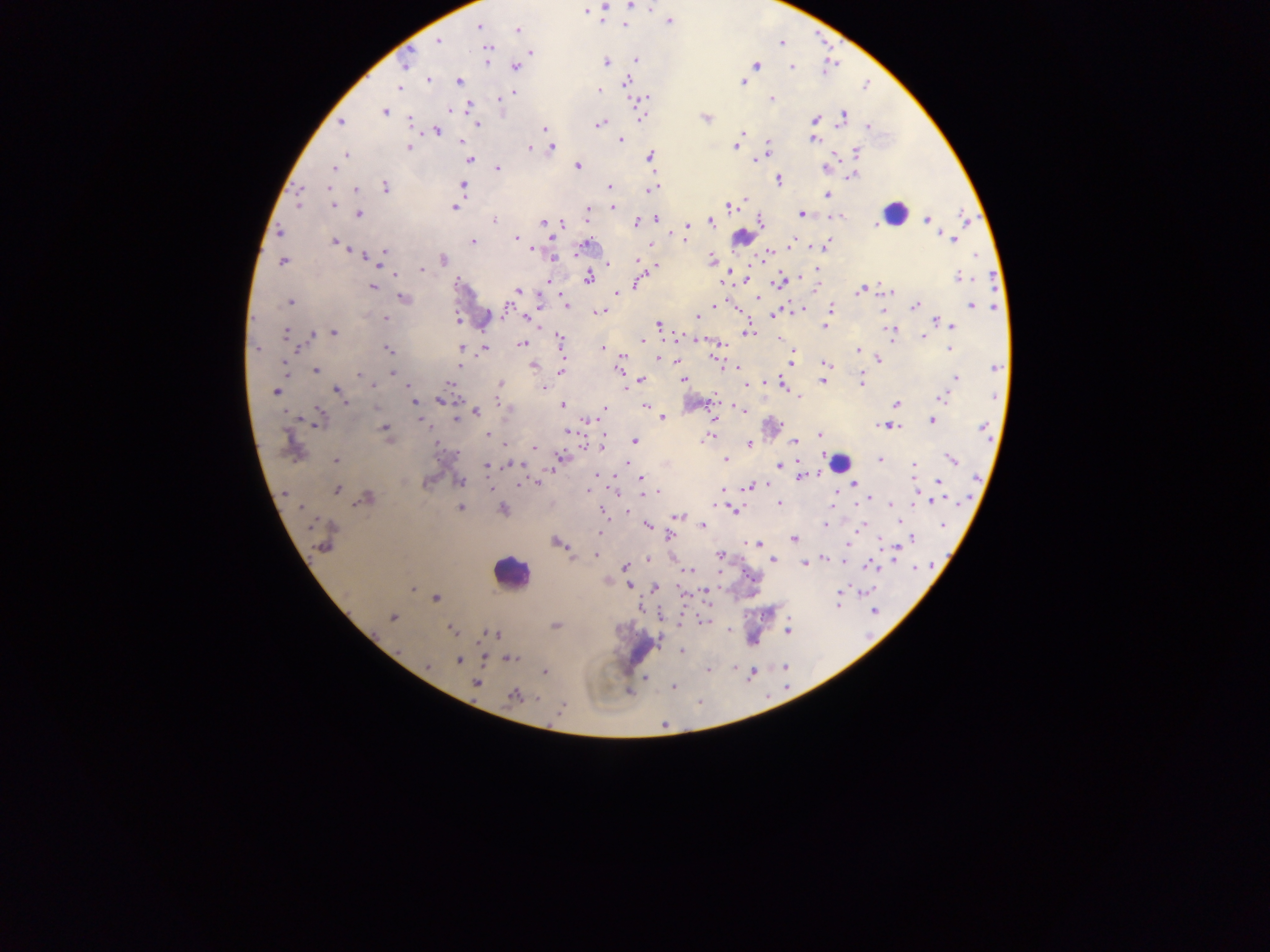

capture = mobile-phone photograph through a microscope
preparation = thick blood smear
field of view = single
image size = 1270×952 pixels
country = Ghana
leukocyte locations = approximate centers as x y in pixels (subset; some below the resolvable size): 896 214; 742 238; 478 310; 841 462; 511 572; 642 650
malaria parasite locations = approximate centers as x y in pixels: 634 5; 604 7; 585 11; 670 21; 625 24; 478 27; 518 29; 438 40; 485 44; 487 52; 531 52; 635 59; 487 60; 405 62; 605 62; 757 65; 516 67; 792 67; 428 80; 459 81; 626 82; 743 82; 399 88; 598 91; 513 93; 503 97; 772 98; 645 99; 468 107; 384 111; 450 111; 640 114; 843 115; 705 118; 814 119; 341 122; 409 122; 477 124; 600 124; 869 126; 544 128; 437 130; 741 132; 622 140; 813 140; 461 142; 767 144; 735 146; 408 147; 529 148; 552 148; 856 152; 346 154; 649 157; 760 157; 470 159; 756 159; 578 166; 334 168; 497 168; 826 168; 854 175; 779 180; 463 185; 329 186; 386 187; 609 188; 356 189; 651 190; 827 195; 297 203; 333 206; 730 206; 455 207; 612 207; 588 212; 359 214; 801 214; 840 216; 655 219; 964 219; 927 220; 494 221; 544 222; 637 222; 711 222; 760 222; 562 223; 877 224; 687 225; 280 232; 685 238; 516 239; 953 239; 475 241; 336 242; 792 243; 586 245; 650 245; 826 245; 532 250; 385 252; 766 254; 364 255; 553 258; 711 259; 443 260; 638 260; 282 261; 608 264; 654 266; 421 270; 395 274; 960 277; 588 278; 548 280; 746 280; 457 281; 778 282; 637 283; 372 287; 814 288; 885 289; 859 290; 518 291; 889 292; 616 293; 403 298; 757 298; 290 302; 566 305; 915 305; 973 305; 714 306; 738 309; 830 309; 505 311; 602 311; 883 311; 773 315; 529 317; 696 317; 386 318; 456 321; 658 325; 949 325; 824 326; 890 331; 334 333; 748 333; 285 334; 312 335; 923 336; 680 338; 780 338; 561 339; 642 340; 522 343; 258 348; 462 348; 484 348; 602 348; 950 349; 388 350; 857 350; 621 357; 658 358; 715 358; 878 360; 677 362; 792 362; 285 364; 825 364; 459 367; 534 367; 996 367; 736 368; 619 370; 315 371; 562 371; 392 372; 358 375; 362 375; 956 378; 684 379; 641 380; 823 381; 862 382; 449 383; 501 383; 782 384; 373 385; 746 385; 409 387; 544 387; 337 390; 275 391; 799 396; 942 398; 439 400; 414 402; 498 402; 346 403; 896 403; 563 405; 646 407; 605 408; 741 410; 475 411; 663 417; 456 418; 419 419; 714 419; 586 421; 931 421; 319 422; 886 426; 893 427; 385 428; 983 428; 567 432; 819 434; 487 435; 711 436; 633 441; 794 441; 749 444; 601 446; 535 447; 561 457; 951 459; 335 460; 726 460; 880 460; 516 465; 779 465; 485 466; 914 466; 597 474; 800 476; 641 478; 940 481; 460 482; 537 483; 521 484; 855 484; 749 486; 489 487; 337 490; 591 490; 722 490; 653 492; 645 493; 286 494; 366 498; 936 500; 716 504; 779 504; 892 505; 460 508; 503 509; 734 511; 679 517; 943 524; 647 525; 703 525; 825 525; 862 526; 600 532; 670 535; 794 538; 912 538; 557 542; 756 543; 324 546; 894 554; 597 555; 720 555; 573 558; 823 558; 647 560; 773 560; 844 560; 805 563; 871 566; 625 567; 916 568; 690 570; 629 586; 413 588; 656 588; 707 591; 866 591; 840 593; 436 598; 837 602; 874 612; 393 618; 703 620; 556 626; 452 630; 728 630; 788 631; 494 634; 399 651; 682 651; 511 659; 459 660; 428 666; 784 667; 708 671; 544 673; 646 678; 476 684; 673 686; 515 697; 561 708